Identify the cell.
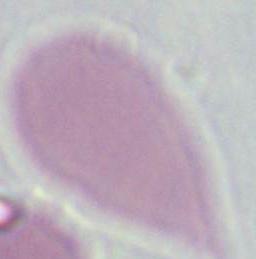

An erythrocyte.

Micrograph. 1000x magnification.